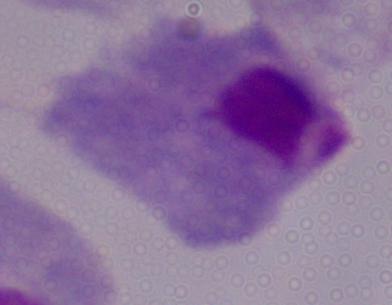

Photomicrograph. A trichomonad is shown. Captured at 1000x magnification.